Describe the morphology of the red blood cells.
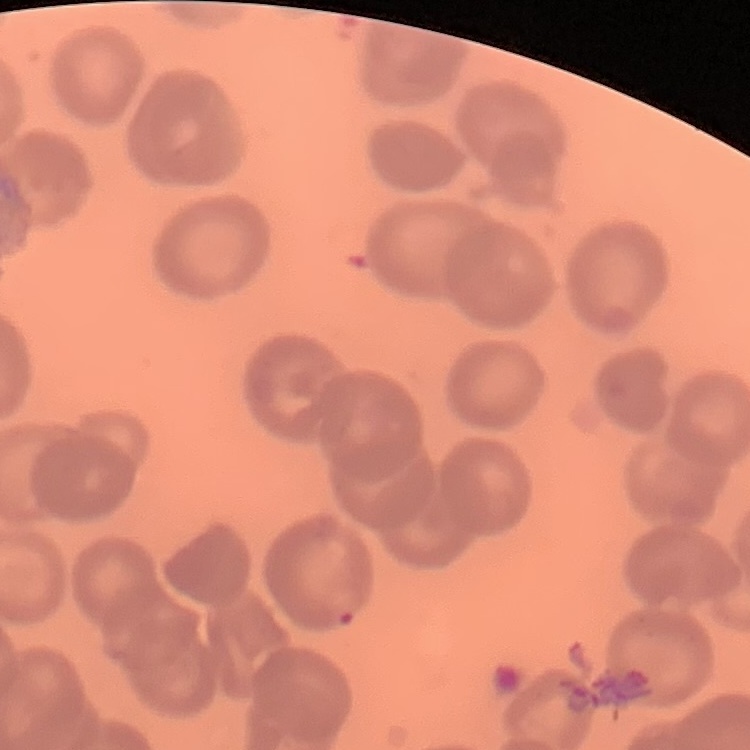

They show no rouleaux formation.

Square crop of a larger photomicrograph. Stained with either Field's or Giemsa. Thin peripheral smear.